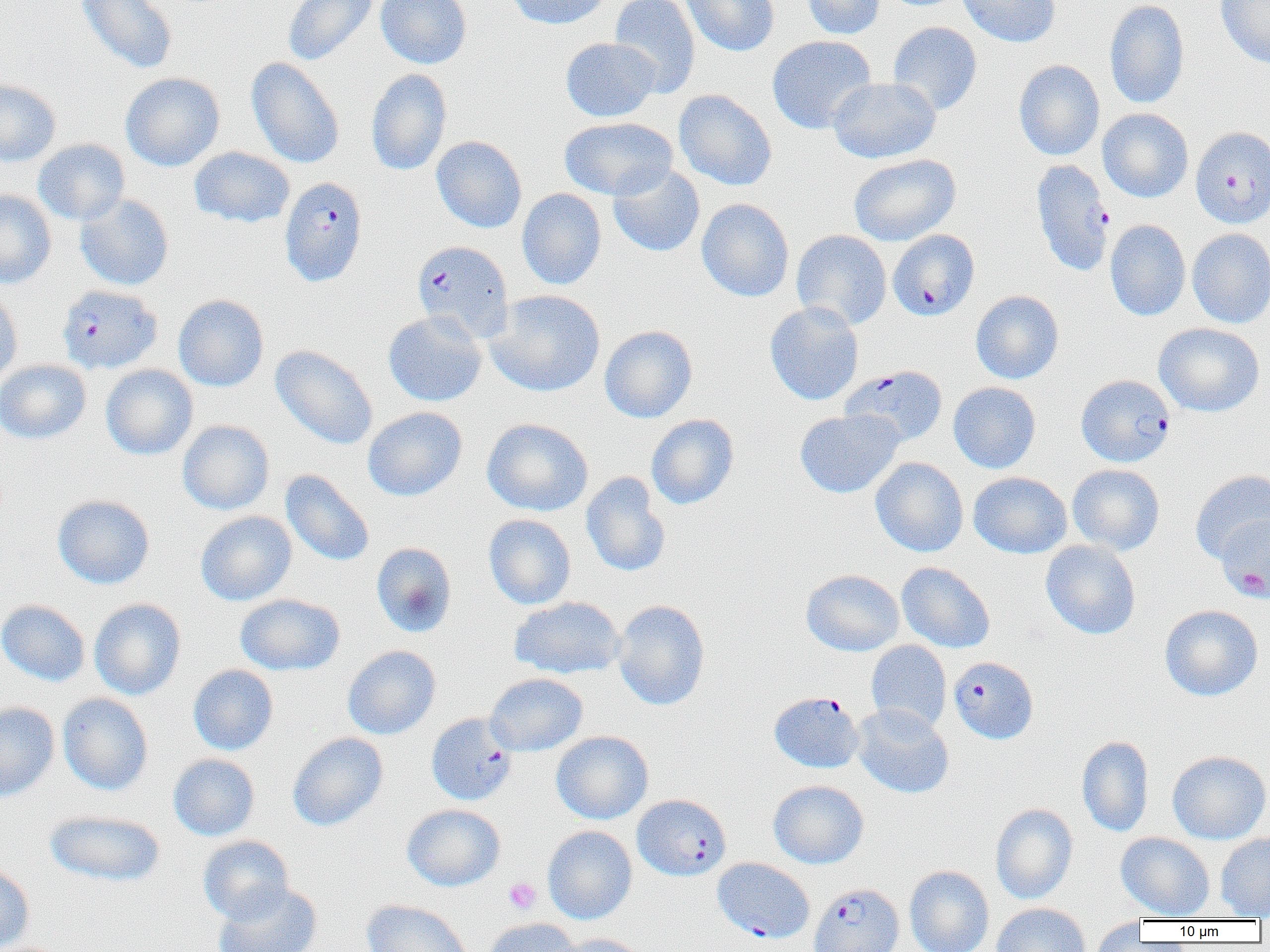
{
  "slide_level_diagnosis": "Plasmodium falciparum",
  "magnification": "1000x",
  "field_of_view": "single",
  "modality": "light microscopy",
  "image_size": "1270×952 pixels",
  "plasmodium_falciparum_infected_red_blood_cell_locations_subset": "approximate bounding boxes as named x1/y1/x2/y2 corners in pixels: (x1=1190, y1=126, x2=1270, y2=228), (x1=1031, y1=160, x2=1114, y2=276), (x1=280, y1=176, x2=367, y2=287), (x1=412, y1=240, x2=513, y2=342), (x1=57, y1=284, x2=162, y2=374), (x1=842, y1=364, x2=947, y2=447), (x1=1076, y1=374, x2=1175, y2=466), (x1=949, y1=656, x2=1038, y2=744), (x1=769, y1=691, x2=863, y2=773), (x1=432, y1=719, x2=523, y2=812), (x1=632, y1=794, x2=731, y2=881), (x1=809, y1=883, x2=903, y2=952)",
  "platelet_locations": "approximate bounding boxes as named x1/y1/x2/y2 corners in pixels: (x1=1231, y1=566, x2=1269, y2=600), (x1=504, y1=877, x2=541, y2=914)",
  "uninfected_red_blood_cell_locations_subset": "approximate bounding boxes as named x1/y1/x2/y2 corners in pixels: (x1=76, y1=0, x2=178, y2=74), (x1=283, y1=0, x2=380, y2=66), (x1=376, y1=0, x2=472, y2=68), (x1=506, y1=0, x2=612, y2=29), (x1=609, y1=0, x2=700, y2=97), (x1=679, y1=0, x2=779, y2=56), (x1=802, y1=0, x2=885, y2=39), (x1=956, y1=0, x2=1060, y2=47), (x1=1104, y1=0, x2=1190, y2=109), (x1=1216, y1=0, x2=1270, y2=68), (x1=888, y1=22, x2=982, y2=116), (x1=767, y1=35, x2=876, y2=134), (x1=560, y1=37, x2=660, y2=122), (x1=246, y1=57, x2=344, y2=168), (x1=1013, y1=59, x2=1105, y2=161), (x1=366, y1=68, x2=452, y2=176), (x1=120, y1=72, x2=225, y2=171), (x1=828, y1=77, x2=941, y2=164), (x1=0, y1=78, x2=61, y2=167), (x1=674, y1=90, x2=777, y2=191), (x1=1098, y1=108, x2=1193, y2=203), (x1=559, y1=117, x2=677, y2=200), (x1=431, y1=136, x2=527, y2=233), (x1=33, y1=139, x2=129, y2=225), (x1=189, y1=147, x2=294, y2=227), (x1=849, y1=154, x2=961, y2=246), (x1=608, y1=163, x2=705, y2=257), (x1=516, y1=188, x2=606, y2=290), (x1=0, y1=190, x2=56, y2=289), (x1=75, y1=194, x2=174, y2=290), (x1=696, y1=198, x2=794, y2=302), (x1=1104, y1=220, x2=1190, y2=321), (x1=1187, y1=228, x2=1270, y2=328), (x1=791, y1=230, x2=892, y2=330), (x1=0, y1=289, x2=23, y2=390), (x1=486, y1=289, x2=606, y2=396), (x1=971, y1=290, x2=1064, y2=384), (x1=173, y1=294, x2=269, y2=391), (x1=765, y1=301, x2=864, y2=406), (x1=383, y1=311, x2=487, y2=406), (x1=1154, y1=322, x2=1264, y2=417), (x1=599, y1=325, x2=697, y2=423), (x1=270, y1=344, x2=378, y2=449), (x1=0, y1=360, x2=91, y2=444), (x1=100, y1=365, x2=198, y2=460), (x1=948, y1=382, x2=1041, y2=473), (x1=362, y1=407, x2=467, y2=501), (x1=795, y1=409, x2=903, y2=498), (x1=646, y1=414, x2=739, y2=509), (x1=482, y1=418, x2=594, y2=516), (x1=177, y1=420, x2=275, y2=515), (x1=870, y1=457, x2=968, y2=557), (x1=1067, y1=464, x2=1165, y2=555), (x1=280, y1=469, x2=375, y2=566), (x1=1190, y1=470, x2=1270, y2=564), (x1=968, y1=471, x2=1072, y2=558), (x1=581, y1=472, x2=671, y2=577), (x1=52, y1=494, x2=155, y2=589), (x1=195, y1=511, x2=296, y2=606), (x1=483, y1=514, x2=576, y2=609), (x1=1216, y1=516, x2=1270, y2=602), (x1=1040, y1=540, x2=1141, y2=639), (x1=371, y1=542, x2=457, y2=638), (x1=896, y1=562, x2=995, y2=653), (x1=801, y1=569, x2=904, y2=656), (x1=235, y1=593, x2=345, y2=675), (x1=509, y1=597, x2=626, y2=679), (x1=89, y1=598, x2=186, y2=700), (x1=0, y1=599, x2=90, y2=686), (x1=612, y1=599, x2=710, y2=711), (x1=1159, y1=605, x2=1262, y2=701), (x1=866, y1=640, x2=951, y2=733), (x1=342, y1=645, x2=441, y2=739), (x1=188, y1=664, x2=279, y2=755), (x1=485, y1=673, x2=587, y2=756), (x1=57, y1=693, x2=153, y2=795), (x1=0, y1=702, x2=60, y2=802), (x1=852, y1=703, x2=953, y2=799), (x1=551, y1=731, x2=653, y2=824), (x1=287, y1=732, x2=388, y2=831), (x1=1077, y1=735, x2=1154, y2=837), (x1=1167, y1=750, x2=1270, y2=844), (x1=168, y1=753, x2=260, y2=841), (x1=768, y1=780, x2=869, y2=869), (x1=402, y1=803, x2=505, y2=891), (x1=991, y1=803, x2=1078, y2=904), (x1=44, y1=810, x2=166, y2=887), (x1=542, y1=825, x2=637, y2=924), (x1=1116, y1=832, x2=1215, y2=920), (x1=1215, y1=833, x2=1270, y2=919), (x1=197, y1=835, x2=294, y2=925), (x1=0, y1=864, x2=35, y2=952), (x1=904, y1=865, x2=994, y2=952), (x1=211, y1=882, x2=321, y2=952), (x1=361, y1=899, x2=473, y2=952), (x1=991, y1=902, x2=1091, y2=952), (x1=484, y1=918, x2=581, y2=952), (x1=1089, y1=918, x2=1148, y2=952), (x1=554, y1=933, x2=649, y2=952)",
  "preparation": "thin blood smear"
}